Assess this cell for malaria.
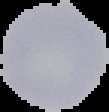

Uninfected.

Image is 109×112 pixels. From a thin blood smear. The area outside the segmented cell region is set to black.